State which cell type is depicted.
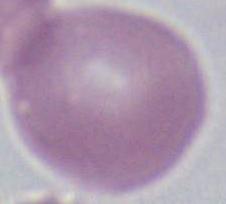
An erythrocyte.

1000x magnification. Micrograph.